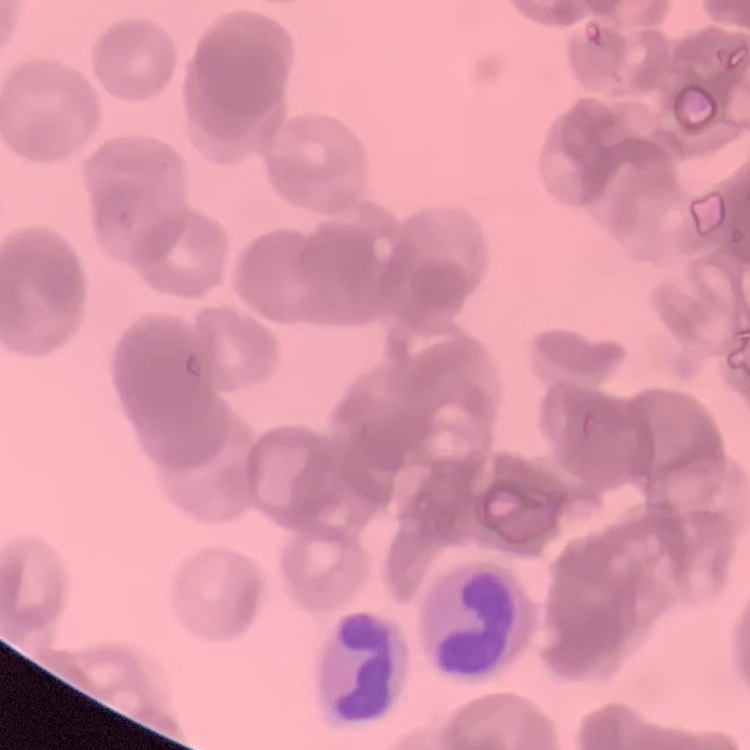

The erythrocytes exhibit rouleaux formation. Field's or Giemsa stain. Square crop of a larger photomicrograph. Thin blood smear.